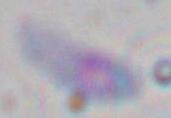

{
  "modality": "photomicrograph",
  "identification": "Toxoplasma gondii",
  "magnification": "1000x"
}